Comment on the morphology of the red blood cells.
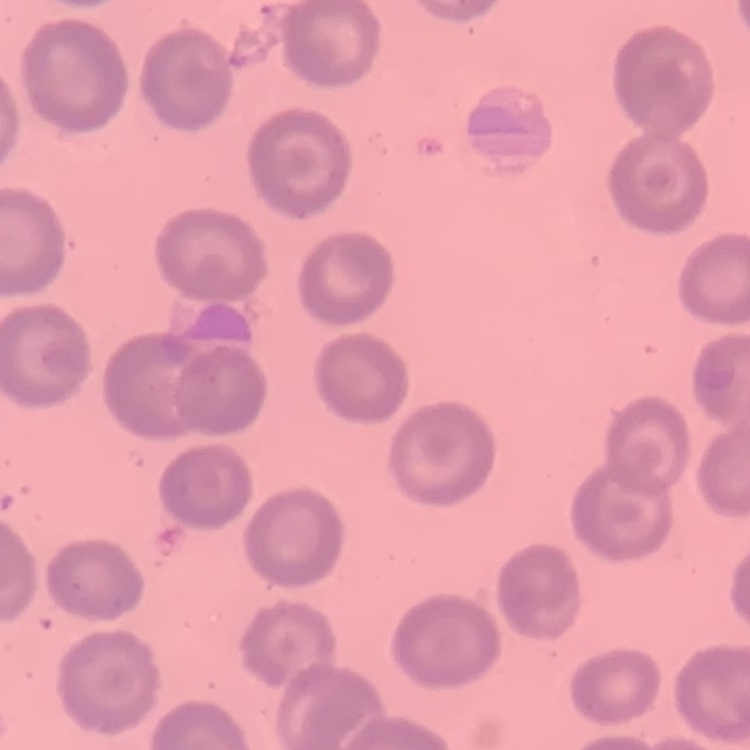
They show no rouleaux formation.

Summary:
  - Image type: square crop of a larger photomicrograph
  - Stain: Field's or Giemsa
  - Preparation: thin blood smear